Outline each Plasmodium vivax-infected red blood cell.
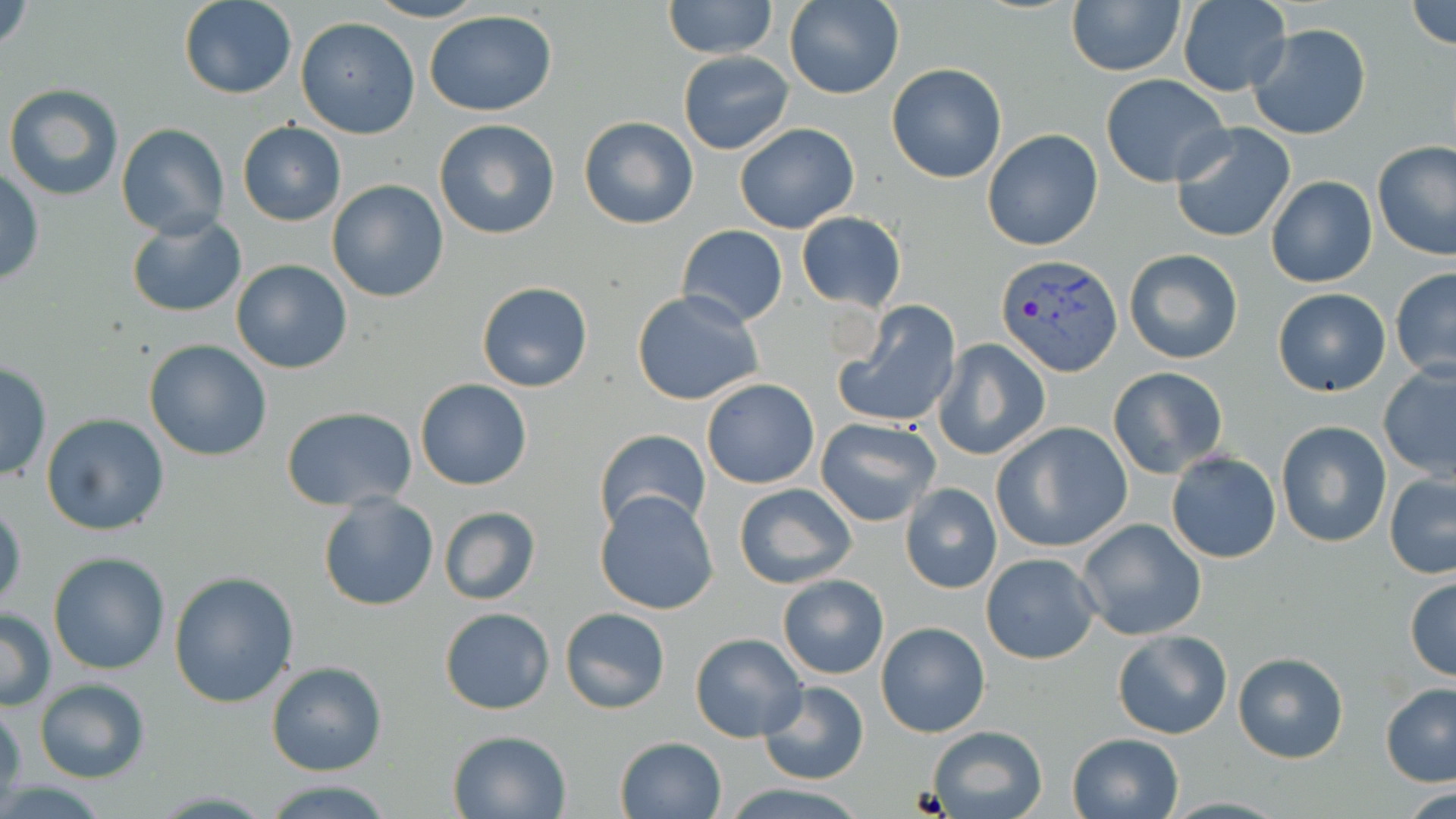

Approximate bounding boxes as [x1, y1, x2, y2] in pixels.
Plasmodium vivax-infected red blood cells: [998, 256, 1124, 379].

Summary:
  - Uninfected red blood cell locations: [2, 0, 34, 57], [366, 0, 488, 23], [663, 0, 778, 60], [785, 0, 905, 100], [1064, 0, 1186, 76], [178, 1, 300, 100], [1406, 1, 1455, 50], [1177, 2, 1291, 95], [425, 9, 557, 118], [296, 17, 420, 138], [1247, 23, 1372, 138], [677, 52, 795, 155], [886, 62, 1008, 183], [1101, 73, 1231, 188], [3, 84, 124, 201], [578, 115, 699, 230], [433, 118, 561, 240], [237, 121, 346, 226], [734, 121, 859, 233], [1169, 121, 1297, 244], [116, 123, 229, 239], [982, 128, 1104, 251], [1373, 141, 1456, 260], [0, 168, 45, 287], [1265, 174, 1377, 288], [326, 181, 451, 302], [796, 212, 907, 311], [125, 215, 247, 318], [677, 225, 787, 328], [1124, 248, 1245, 365], [230, 258, 353, 374], [1390, 267, 1456, 380], [477, 281, 594, 393], [1272, 288, 1390, 397], [630, 291, 767, 406], [834, 299, 963, 430], [935, 337, 1049, 459], [143, 339, 273, 462], [0, 361, 51, 483], [1378, 361, 1456, 481], [1107, 366, 1229, 478], [701, 377, 820, 489], [415, 379, 533, 490], [281, 406, 418, 510], [40, 414, 169, 536], [815, 417, 942, 527], [1276, 420, 1392, 548], [992, 422, 1134, 553], [593, 430, 710, 535], [1165, 451, 1282, 564], [1385, 474, 1456, 579], [733, 483, 857, 588], [901, 483, 1001, 594], [595, 492, 718, 615], [316, 494, 438, 611], [0, 499, 25, 618], [438, 506, 541, 604], [1076, 519, 1208, 642], [48, 552, 171, 675], [981, 553, 1101, 665], [169, 570, 298, 707], [776, 575, 888, 680], [1404, 576, 1456, 682], [559, 607, 670, 714], [0, 608, 55, 711], [438, 608, 554, 715], [876, 621, 989, 738], [1112, 630, 1232, 739], [690, 632, 808, 743], [1232, 650, 1350, 763], [265, 661, 387, 777], [34, 679, 152, 784], [756, 680, 869, 786], [1381, 684, 1456, 788], [0, 702, 24, 806], [925, 725, 1049, 819], [446, 729, 571, 819], [1067, 733, 1183, 819], [615, 735, 725, 818], [258, 779, 401, 818], [721, 781, 864, 817]
  - Platelet locations: [911, 788, 952, 815]
  - Slide-level diagnosis: Plasmodium vivax
  - Modality: optical microscopy
  - Image size: 1456×819 pixels
  - Magnification: 1000x
  - Preparation: thin blood smear
  - Stain: May-Grünwald-Giemsa
  - Field of view: single